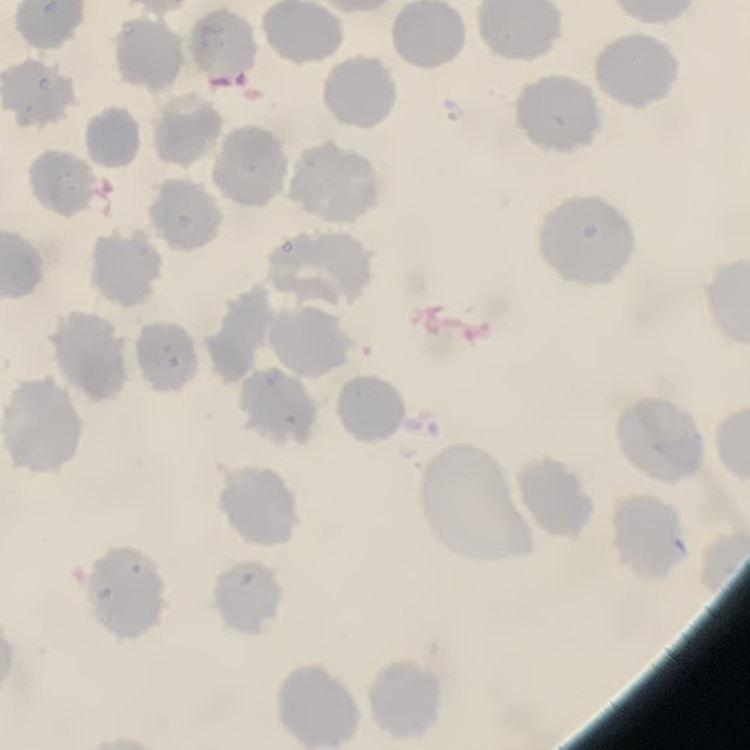
red blood cell morphology = no rouleaux formation
preparation = thin peripheral smear
image type = square crop of a larger photomicrograph
stain = Field's or Giemsa